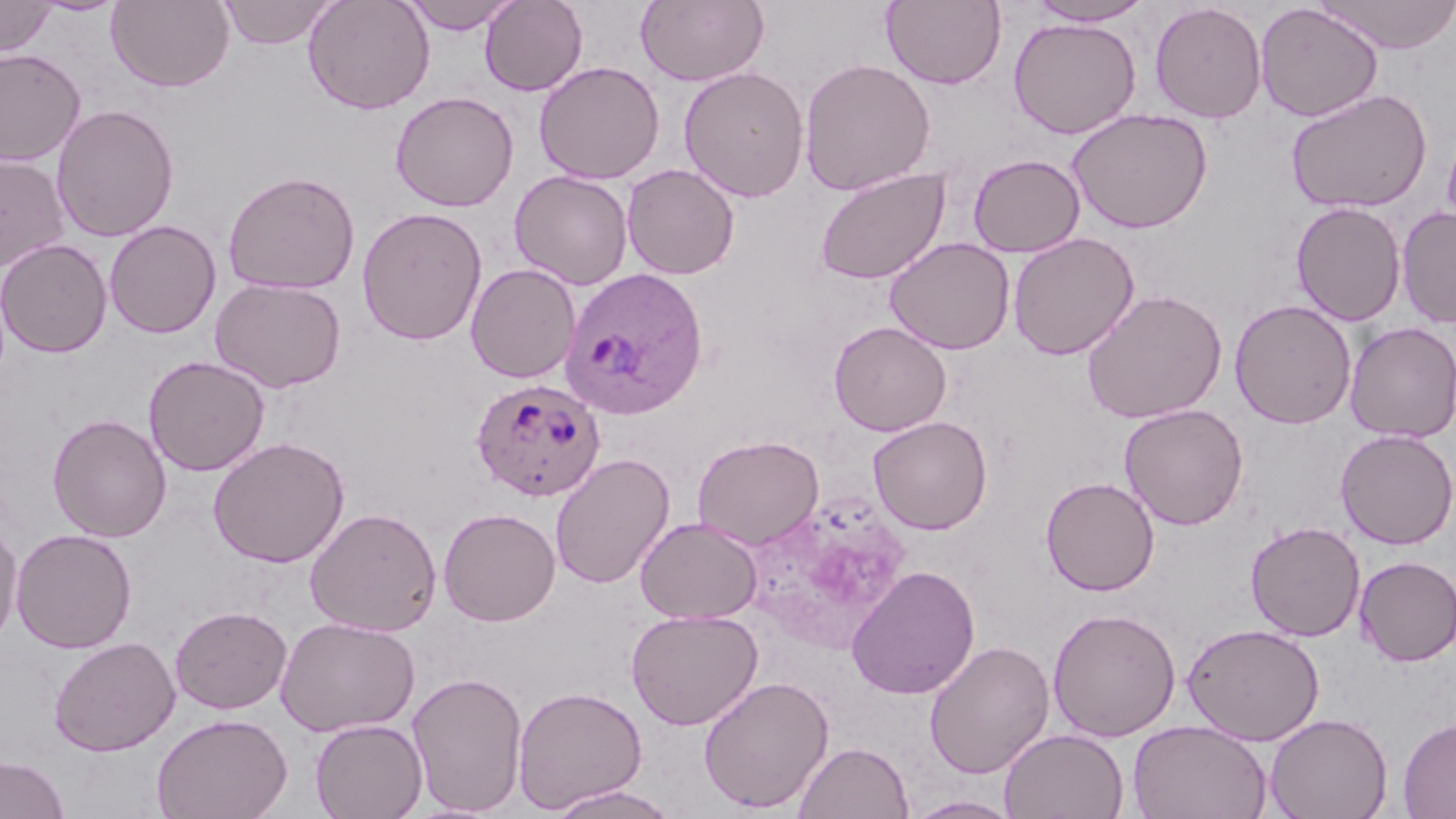

Summary:
  - Coordinate format: approximate bounding boxes as [x1, y1, x2, y2] in pixels
  - Uninfected red blood cell locations: [0, 0, 58, 57], [106, 0, 234, 92], [217, 0, 340, 49], [303, 0, 435, 115], [400, 0, 521, 34], [479, 0, 588, 96], [636, 0, 770, 87], [881, 0, 1008, 90], [1025, 0, 1156, 27], [1314, 0, 1456, 53], [1149, 2, 1267, 123], [1255, 3, 1383, 122], [1007, 17, 1142, 138], [0, 48, 87, 167], [799, 57, 936, 196], [533, 60, 666, 184], [678, 65, 810, 202], [1285, 88, 1433, 214], [389, 90, 520, 212], [51, 104, 179, 242], [1067, 108, 1214, 234], [0, 153, 71, 271], [967, 154, 1085, 257], [622, 164, 740, 280], [814, 167, 951, 285], [508, 169, 634, 290], [221, 170, 361, 294], [1291, 202, 1406, 326], [356, 207, 488, 345], [1397, 207, 1456, 329], [104, 220, 221, 338], [1008, 232, 1140, 360], [884, 237, 1015, 355], [0, 238, 113, 358], [465, 263, 581, 384], [209, 277, 347, 393], [1081, 288, 1228, 424], [1229, 298, 1357, 429], [829, 321, 952, 436], [1344, 322, 1456, 443], [143, 355, 270, 476], [1119, 403, 1249, 530], [47, 413, 172, 543], [868, 415, 993, 535], [1335, 428, 1456, 550], [692, 435, 824, 550], [208, 436, 349, 567], [550, 453, 675, 590], [1040, 476, 1160, 596], [305, 507, 442, 637], [437, 507, 561, 626], [635, 516, 762, 624], [0, 517, 23, 648], [1245, 521, 1366, 641], [10, 528, 137, 653], [1355, 555, 1456, 666], [846, 565, 980, 699], [170, 605, 292, 714], [625, 608, 763, 730], [1047, 608, 1181, 742], [275, 616, 420, 737], [1182, 623, 1325, 745], [49, 636, 180, 757], [923, 640, 1055, 779], [406, 671, 529, 815], [697, 675, 834, 813], [512, 686, 647, 814], [151, 713, 293, 819], [1265, 713, 1393, 819], [1398, 716, 1456, 818], [310, 718, 428, 819], [1128, 720, 1272, 819], [1000, 728, 1129, 818], [793, 741, 914, 819], [0, 755, 70, 819], [543, 785, 682, 819], [903, 795, 1022, 818]
  - Plasmodium ovale-infected red blood cell locations: [560, 267, 709, 420], [470, 377, 607, 502]
  - Slide-level diagnosis: Plasmodium ovale
  - Image size: 1456×819 pixels
  - Stain: May-Grünwald-Giemsa
  - Preparation: thin blood smear
  - Modality: light microscopy
  - Field of view: single
  - Magnification: 1000x